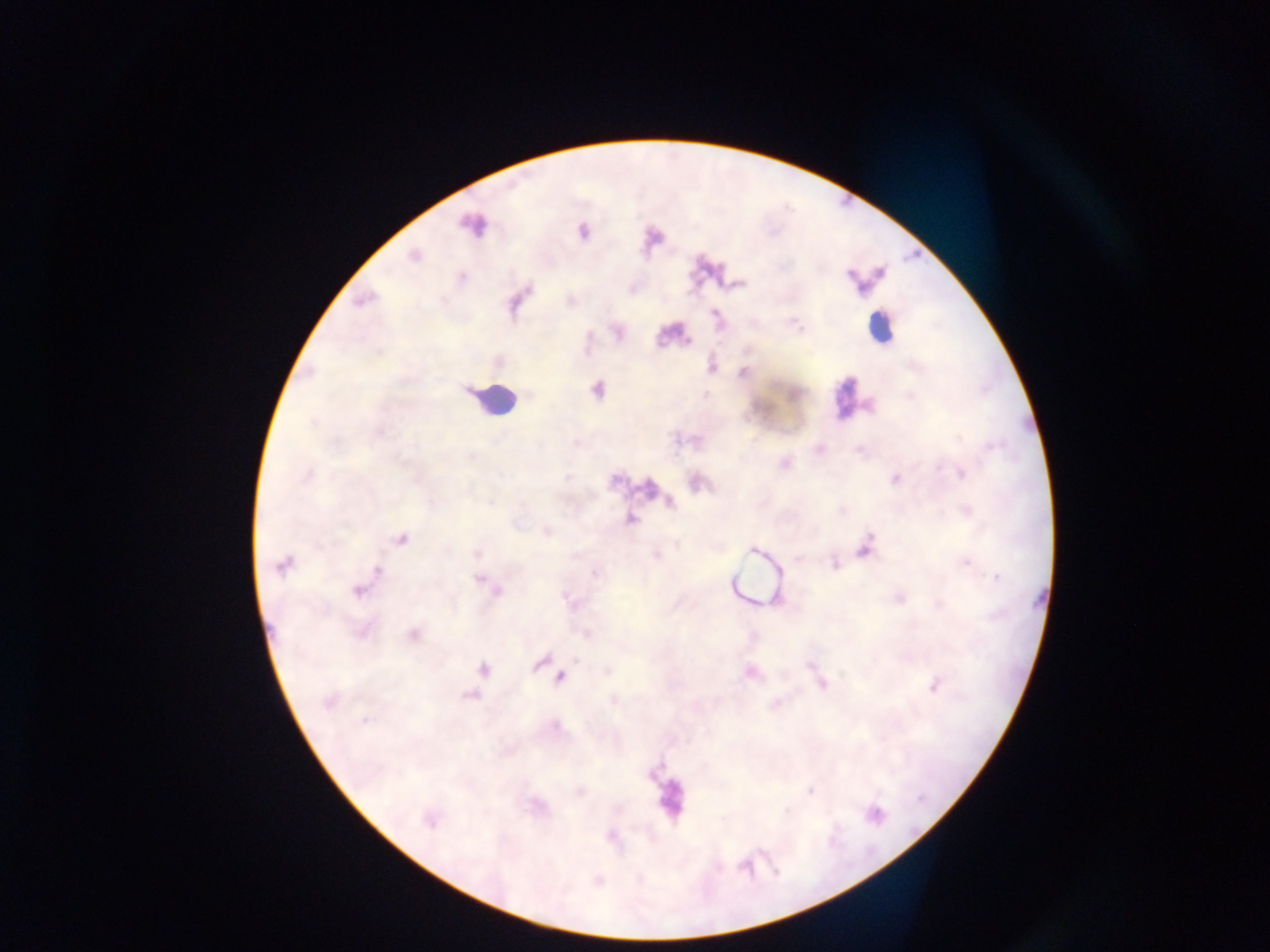
Approximate centers as {x, y} in pixels.
Summary:
  - Leukocyte locations: {875, 329}, {494, 400}, {851, 400}, {668, 799}
  - Malaria parasite locations: {472, 225}, {583, 232}, {414, 256}, {880, 272}, {849, 275}, {462, 277}, {364, 299}, {744, 373}, {597, 391}, {960, 474}, {307, 475}, {895, 480}, {671, 503}, {631, 519}, {401, 539}, {865, 547}, {753, 550}, {476, 553}, {834, 563}, {966, 564}, {283, 566}, {378, 571}, {594, 573}, {996, 577}, {479, 580}, {489, 586}, {358, 591}, {496, 591}, {901, 599}, {414, 634}, {540, 663}, {483, 670}, {560, 677}, {820, 682}, {935, 685}, {470, 696}, {328, 703}, {364, 721}, {430, 821}
  - Country: Ghana
  - Image size: 1270×952 pixels
  - Preparation: thick blood film
  - Capture: mobile-phone photograph through a microscope
  - Field of view: single